Outline every malaria parasite, every leukocyte, and every artifact (stain precipitate or debris).
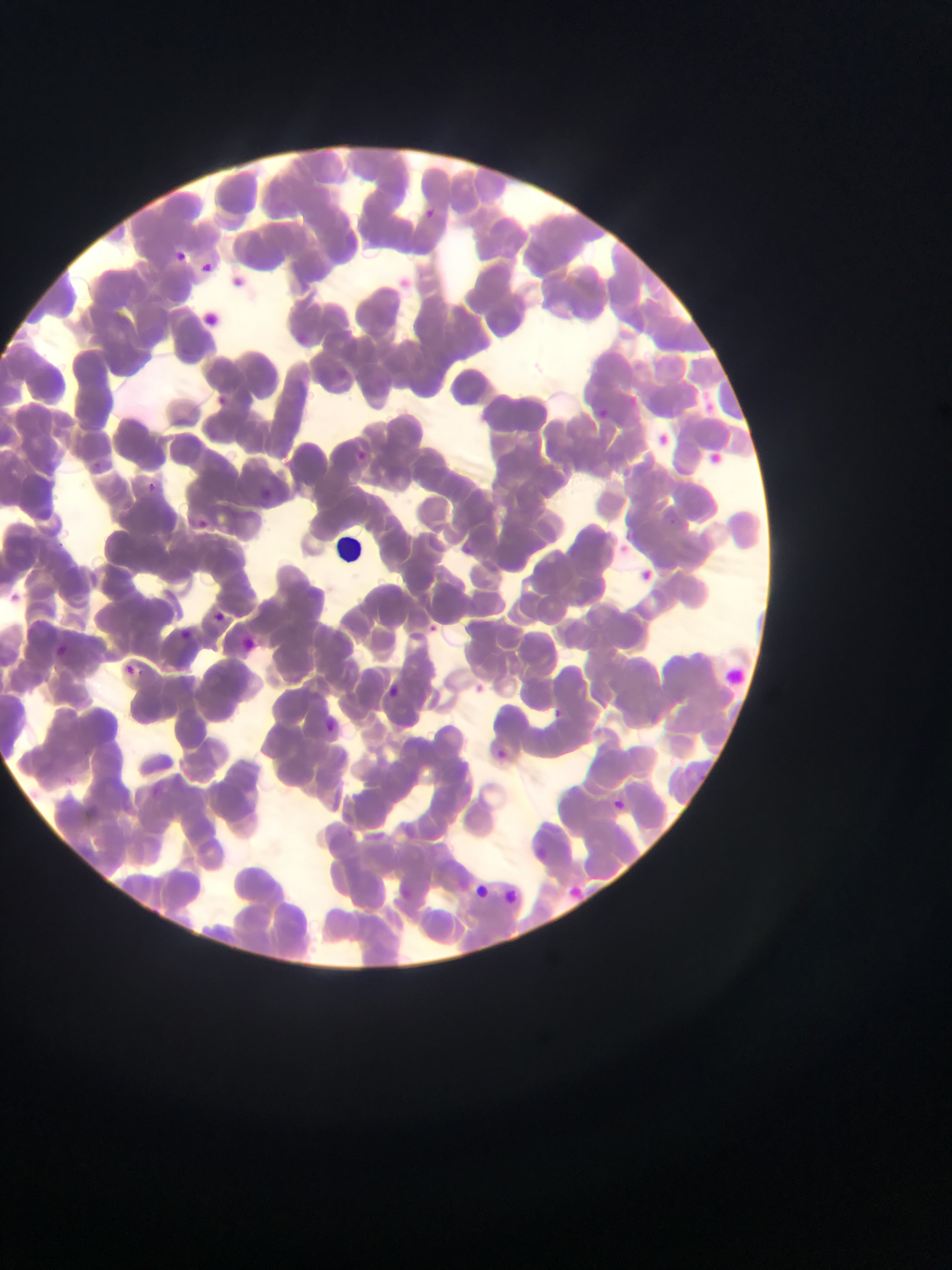

Approximate bounding boxes as (left, top, right, bottom) in pixels.
Malaria parasites: (424, 208, 444, 222), (169, 248, 187, 260), (195, 257, 212, 270), (295, 333, 310, 341), (627, 388, 642, 412), (212, 393, 233, 405), (701, 395, 733, 418), (595, 404, 618, 421), (349, 449, 375, 464), (147, 483, 157, 492), (244, 491, 276, 500), (190, 510, 213, 531), (455, 539, 474, 559), (642, 564, 659, 581), (214, 612, 222, 620), (177, 626, 191, 639), (44, 645, 67, 659), (123, 666, 131, 674), (386, 681, 400, 692), (541, 703, 562, 722), (491, 747, 504, 758), (610, 797, 626, 808), (473, 878, 492, 898), (567, 886, 579, 899), (504, 889, 520, 905).
No leukocytes observed.

Summary:
  - Field of view: single
  - Preparation: thin blood smear
  - Country: Ghana
  - Image size: 952×1270 pixels
  - Capture: mobile-phone photograph through a microscope